Identify the parasite.
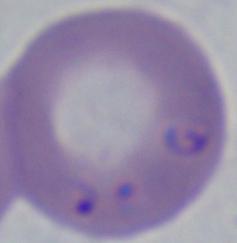
This is Babesia.

Summary:
  - Modality: micrograph
  - Magnification: 1000x